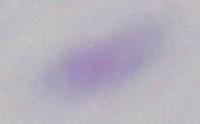
magnification = 1000x
modality = photomicrograph
identification = Toxoplasma gondii